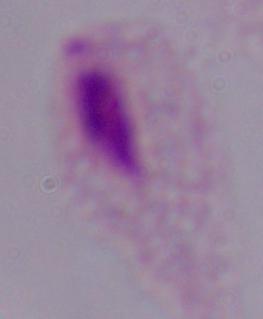

magnification = 1000x
identification = trichomonad
modality = photomicrograph